Outline each blood parasite and name the species.
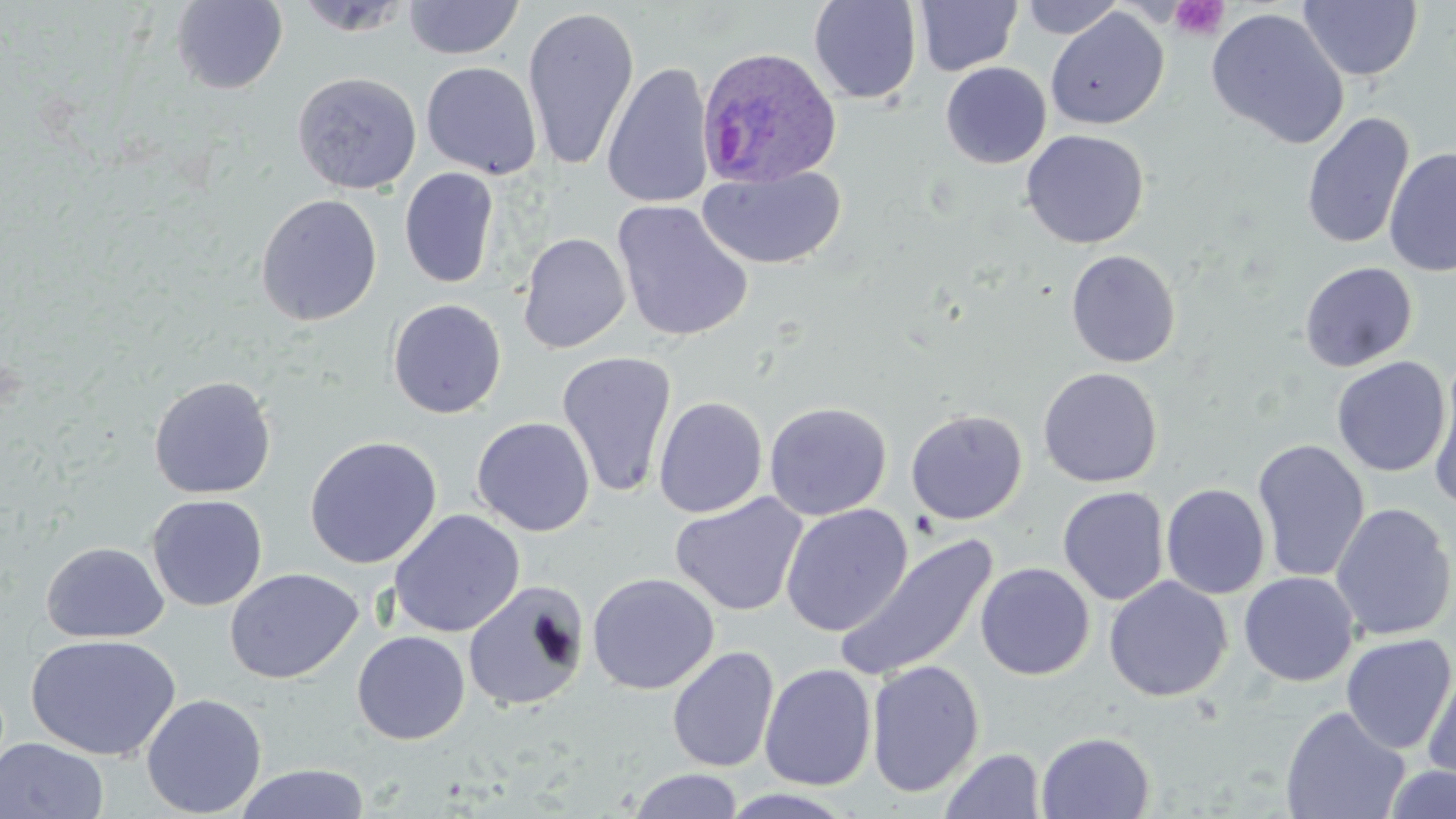

Approximate bounding boxes as [x1, y1, x2, y2] in pixels.
Plasmodium ovale-infected red blood cells: [695, 45, 842, 188].
No Plasmodium falciparum, Plasmodium malariae, Plasmodium vivax, Babesia divergens, or Trypanosoma brucei observed.

Platelet locations: [1169, 1, 1229, 40]. Uninfected red blood cell locations: [403, 0, 524, 60], [1018, 0, 1126, 39], [170, 1, 289, 94], [809, 1, 922, 104], [913, 1, 1022, 76], [1297, 1, 1422, 82], [522, 6, 640, 172], [1045, 8, 1168, 130], [1206, 8, 1349, 149], [420, 61, 543, 179], [602, 61, 714, 210], [940, 62, 1052, 168], [292, 71, 422, 194], [1301, 112, 1415, 250], [1021, 130, 1149, 249], [1384, 146, 1456, 277], [697, 166, 847, 270], [399, 167, 500, 289], [255, 193, 383, 326], [611, 200, 753, 343], [518, 232, 631, 354], [1065, 249, 1181, 368], [1059, 250, 1172, 489], [1299, 262, 1417, 371], [387, 298, 506, 419], [556, 351, 678, 498], [1331, 356, 1452, 477], [1428, 357, 1455, 514], [1038, 367, 1163, 488], [148, 375, 277, 499], [653, 396, 768, 518], [764, 401, 892, 521], [906, 408, 1028, 525], [471, 416, 595, 536], [304, 435, 442, 569], [1252, 439, 1370, 584], [1161, 484, 1271, 599], [1058, 486, 1169, 605], [670, 492, 807, 616], [147, 494, 268, 611], [1330, 502, 1455, 642], [781, 504, 913, 636], [388, 509, 525, 638], [836, 533, 999, 683], [41, 542, 169, 643], [975, 562, 1094, 680], [224, 567, 363, 683], [1238, 571, 1359, 686], [586, 572, 719, 695], [1104, 576, 1232, 702], [463, 579, 589, 712], [351, 630, 470, 745], [25, 633, 181, 761], [1340, 633, 1455, 754], [667, 646, 780, 773], [866, 660, 985, 798], [759, 663, 877, 791], [1422, 664, 1456, 790], [141, 693, 267, 818], [1280, 706, 1410, 819], [1036, 731, 1155, 819], [0, 737, 109, 819], [940, 748, 1045, 819], [234, 763, 370, 819], [1383, 764, 1456, 819], [629, 768, 744, 819], [719, 788, 858, 818]. Slide-level diagnosis: Plasmodium ovale. Image is 1456×819 pixels. Thin blood film. 1000x magnification. Optical microscopy. Single field of view. May-Grünwald-Giemsa stain.